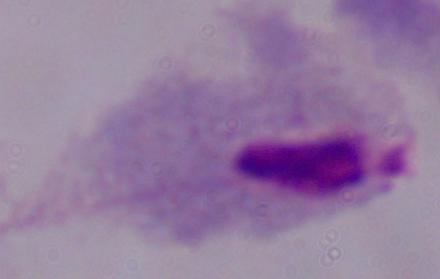

Summary:
  - Modality: micrograph
  - Magnification: 1000x
  - Identification: trichomonad